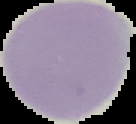

malaria_status: uninfected
image_size: 136×124 pixels
image_type: cell region segmented out of the field of view; surrounding area masked to black
preparation: thin blood film